Identify the parasite.
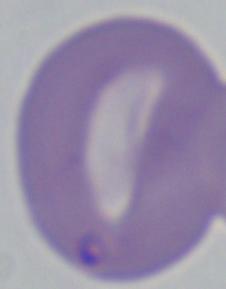

Babesia.

magnification: 1000x
modality: micrograph